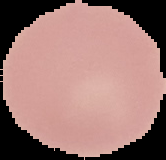
Image is 166×160 pixels. Malaria status: uninfected. The area outside the segmented cell region is set to black. From a thin blood film.